Identify the preparation type.
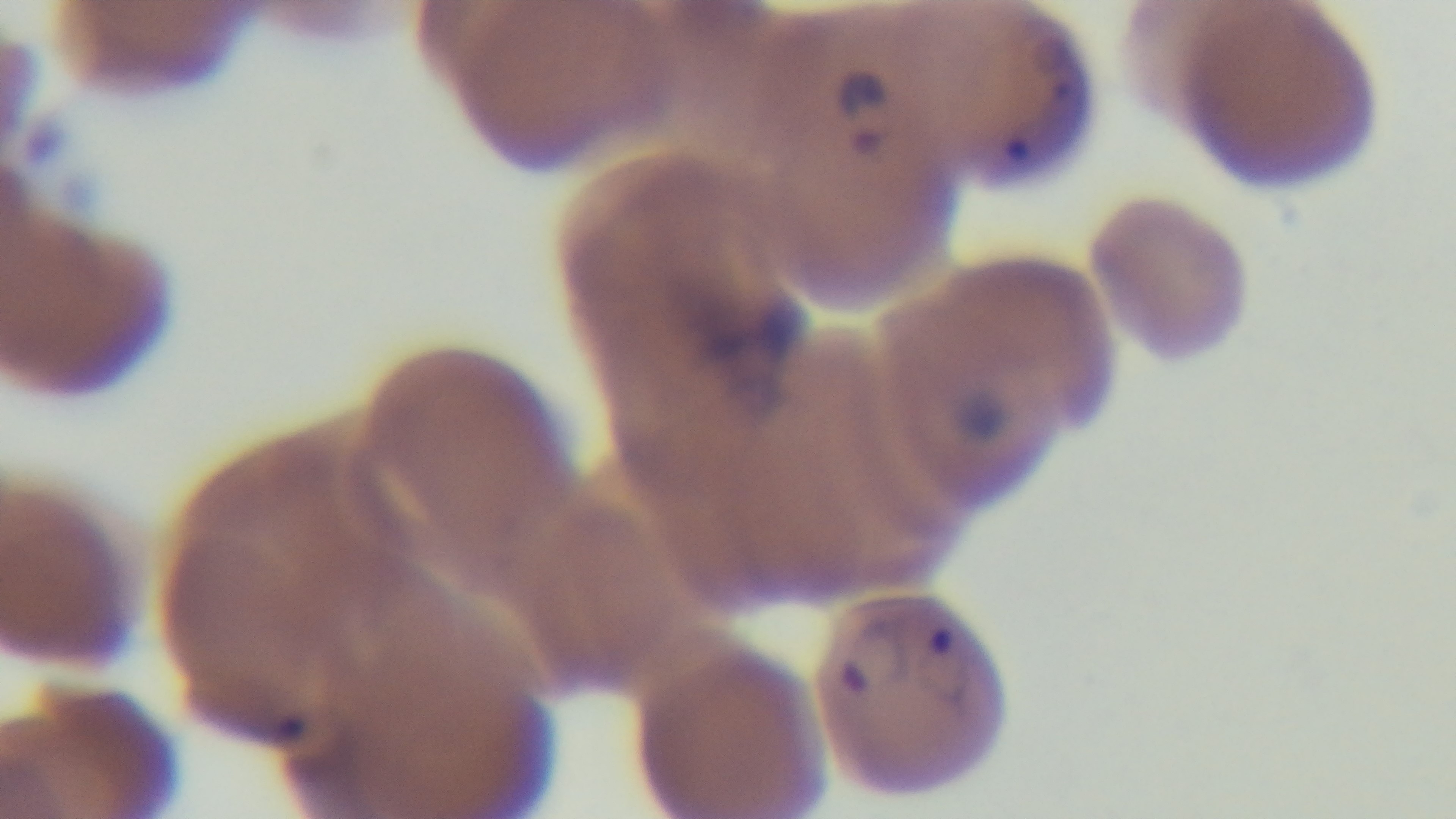
Thin.

objective: 100x oil immersion
field_of_view: one from the slide
capture: mounted 4K digital camera
stain: Giemsa
malaria_status: positive
modality: light microscopy